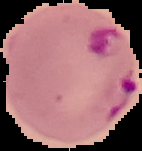

Summary:
  - Preparation: thin blood smear
  - Image type: cell region segmented out of the field of view; surrounding area masked to black
  - Image size: 142×151 pixels
  - Result: Plasmodium parasites identified